Identify the blood parasite species.
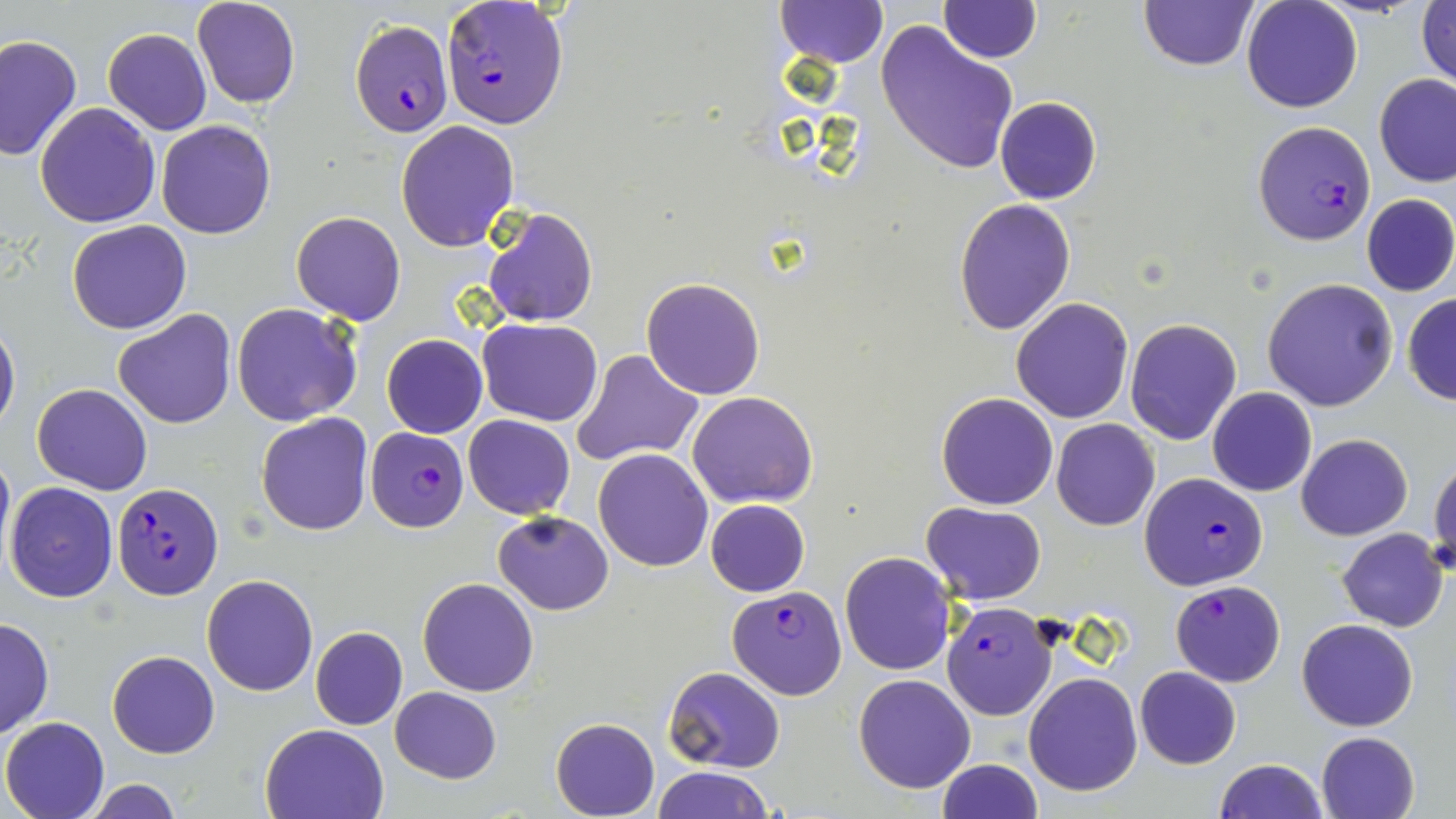

Plasmodium falciparum.

Summary:
  - Coordinate format: approximate bounding boxes as named x1/y1/x2/y2 corners in pixels
  - Plasmodium falciparum-infected red blood cell locations: (x1=442, y1=1, x2=569, y2=129), (x1=349, y1=19, x2=454, y2=135), (x1=1250, y1=121, x2=1375, y2=245), (x1=366, y1=426, x2=467, y2=531), (x1=1139, y1=472, x2=1270, y2=589), (x1=113, y1=482, x2=223, y2=599), (x1=1170, y1=579, x2=1286, y2=686), (x1=728, y1=586, x2=845, y2=697), (x1=942, y1=604, x2=1060, y2=722)
  - Uninfected red blood cell locations: (x1=191, y1=0, x2=300, y2=110), (x1=936, y1=1, x2=1041, y2=63), (x1=1138, y1=1, x2=1258, y2=71), (x1=1241, y1=1, x2=1363, y2=114), (x1=777, y1=2, x2=887, y2=68), (x1=1416, y1=2, x2=1456, y2=91), (x1=875, y1=19, x2=1018, y2=176), (x1=102, y1=28, x2=212, y2=135), (x1=0, y1=33, x2=82, y2=162), (x1=1374, y1=73, x2=1456, y2=187), (x1=995, y1=97, x2=1102, y2=205), (x1=35, y1=103, x2=162, y2=228), (x1=155, y1=120, x2=277, y2=239), (x1=395, y1=120, x2=520, y2=250), (x1=1362, y1=193, x2=1456, y2=297), (x1=954, y1=199, x2=1076, y2=335), (x1=481, y1=206, x2=598, y2=328), (x1=292, y1=211, x2=406, y2=324), (x1=66, y1=220, x2=192, y2=335), (x1=640, y1=277, x2=766, y2=400), (x1=1264, y1=278, x2=1398, y2=412), (x1=1402, y1=294, x2=1456, y2=406), (x1=1010, y1=297, x2=1134, y2=423), (x1=231, y1=302, x2=363, y2=427), (x1=114, y1=309, x2=236, y2=428), (x1=1125, y1=317, x2=1243, y2=445), (x1=479, y1=318, x2=602, y2=424), (x1=0, y1=319, x2=20, y2=433), (x1=381, y1=334, x2=487, y2=438), (x1=573, y1=349, x2=703, y2=467), (x1=32, y1=384, x2=152, y2=495), (x1=1207, y1=388, x2=1316, y2=496), (x1=687, y1=390, x2=818, y2=509), (x1=936, y1=391, x2=1058, y2=510), (x1=472, y1=410, x2=587, y2=613), (x1=256, y1=413, x2=373, y2=535), (x1=462, y1=414, x2=576, y2=518), (x1=1051, y1=419, x2=1160, y2=531), (x1=1295, y1=432, x2=1413, y2=540), (x1=0, y1=444, x2=13, y2=566), (x1=592, y1=447, x2=714, y2=571), (x1=1428, y1=456, x2=1456, y2=579), (x1=5, y1=482, x2=119, y2=602), (x1=705, y1=499, x2=810, y2=596), (x1=923, y1=503, x2=1046, y2=605), (x1=492, y1=509, x2=614, y2=614), (x1=1337, y1=527, x2=1450, y2=632), (x1=839, y1=552, x2=958, y2=675), (x1=201, y1=574, x2=318, y2=695), (x1=417, y1=577, x2=539, y2=696), (x1=0, y1=617, x2=54, y2=739), (x1=1296, y1=617, x2=1418, y2=732), (x1=309, y1=627, x2=408, y2=730), (x1=108, y1=650, x2=220, y2=758), (x1=662, y1=666, x2=785, y2=774), (x1=1135, y1=666, x2=1240, y2=769), (x1=853, y1=673, x2=976, y2=793), (x1=1024, y1=673, x2=1143, y2=794), (x1=389, y1=687, x2=502, y2=783), (x1=1, y1=717, x2=109, y2=819), (x1=551, y1=717, x2=660, y2=819), (x1=259, y1=722, x2=389, y2=819), (x1=1316, y1=730, x2=1420, y2=818), (x1=936, y1=758, x2=1043, y2=819), (x1=1215, y1=759, x2=1327, y2=819), (x1=652, y1=766, x2=772, y2=819), (x1=83, y1=778, x2=184, y2=819)
  - Stain: May-Grünwald-Giemsa
  - Modality: light microscopy
  - Image size: 1456×819 pixels
  - Preparation: thin blood smear
  - Magnification: 1000x
  - Field of view: single